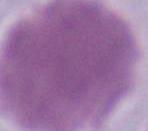

Photomicrograph. 1000x magnification. A red blood cell is shown.